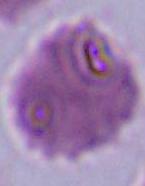
modality = micrograph
magnification = 1000x
identification = red blood cell